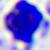 Micrograph. A white blood cell is shown. 400x magnification.